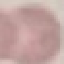

malaria_status: uninfected
preparation: thin blood film
capture: smartphone through the microscope eyepiece
image_type: cell patch, automatically extracted from a larger field of view and resized to 64 × 64 pixels
stain: Giemsa